Identify the parasite.
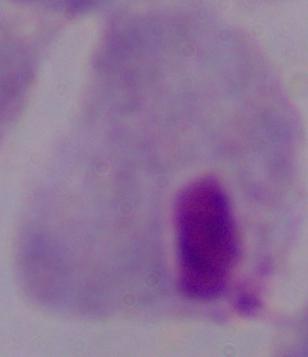
A trichomonad.

Summary:
  - Modality: micrograph
  - Magnification: 1000x